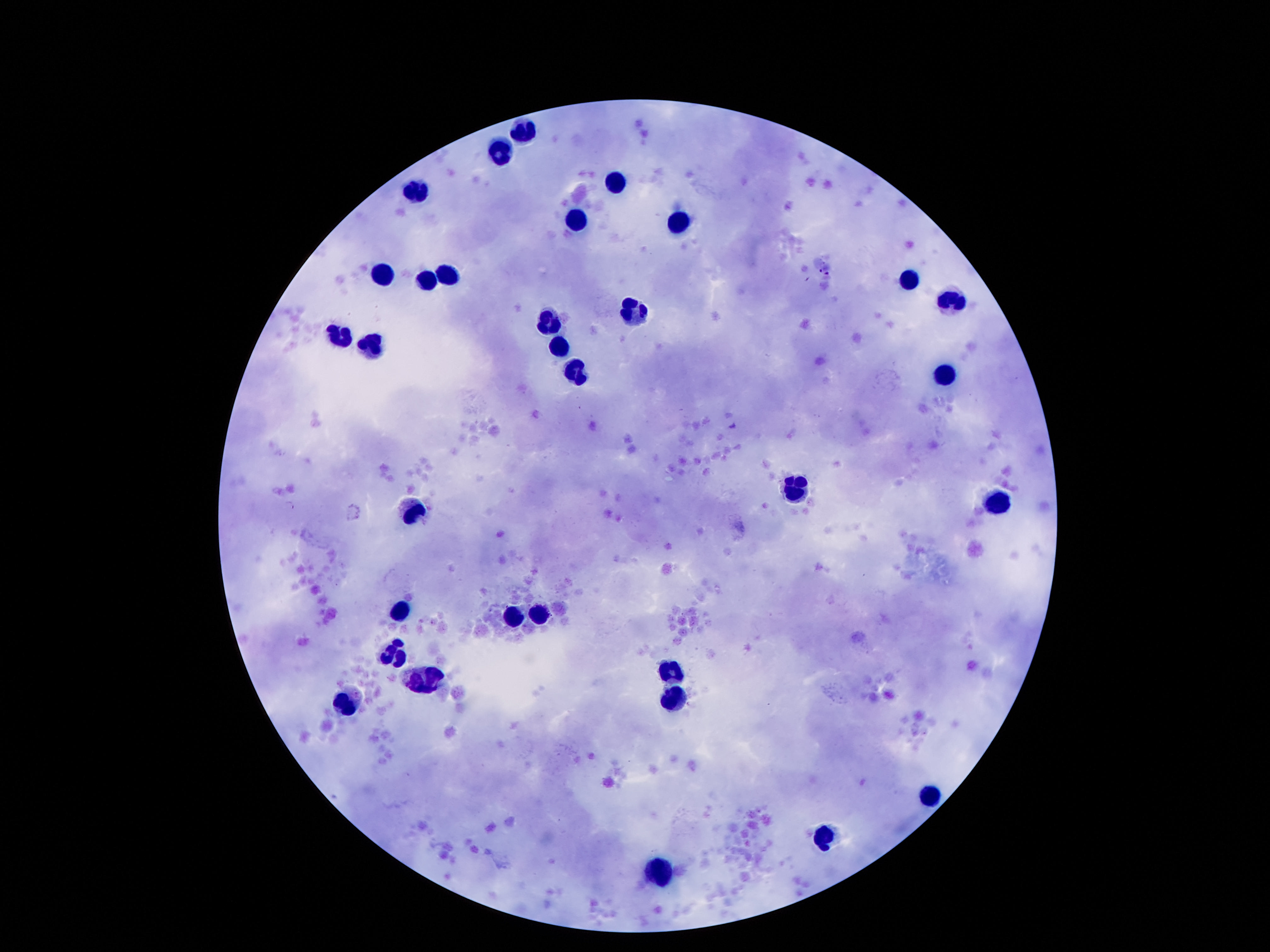

Approximate centers as [x, y] in pixels. Leukocyte locations: [525, 133], [498, 160], [611, 183], [416, 190], [573, 219], [684, 219], [446, 267], [375, 271], [425, 274], [911, 276], [945, 299], [625, 315], [546, 321], [344, 340], [555, 344], [373, 346], [575, 369], [943, 374], [793, 487], [993, 498], [412, 510], [398, 605], [514, 616], [536, 619], [393, 655], [677, 673], [422, 678], [675, 698], [342, 704], [929, 798], [832, 836], [659, 870]. Giemsa stain. Photographed through the microscope eyepiece with a smartphone camera. Single field of view. Patient malaria status: uninfected. Thick peripheral-blood smear. Image is 1270×952 pixels. 100x magnification.